Describe the morphology of the red blood cells.
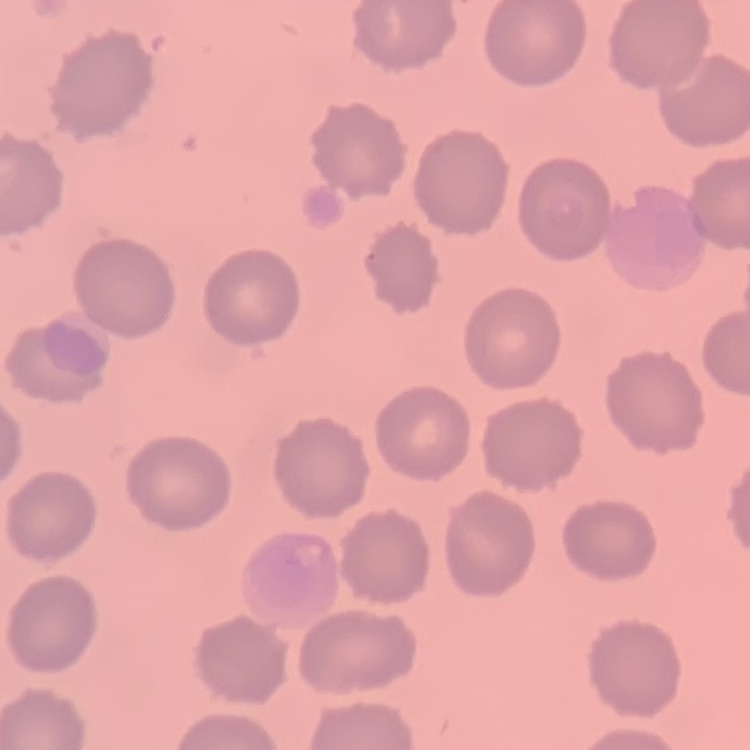

They show no rouleaux formation.

image type = square crop of a larger photomicrograph
stain = Field's or Giemsa
preparation = thin blood film